Point out each malaria parasite.
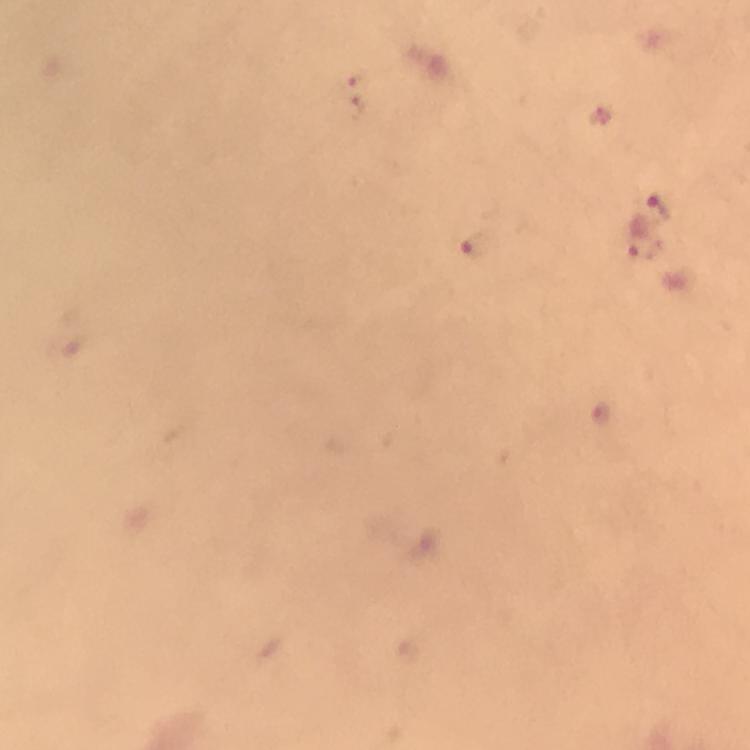

Approximate centers as {x, y} in pixels.
Malaria parasites: {358, 77}, {357, 108}, {661, 207}, {647, 246}, {475, 248}, {603, 415}.

Thick smear. Photographed with a smartphone mounted on the microscope. Immersion oil was used. Image is 750×750 pixels. At 100x magnification. A crop from one field of view. From a malaria diagnostic workup. Giemsa stain.